Describe the morphology of the red blood cells.
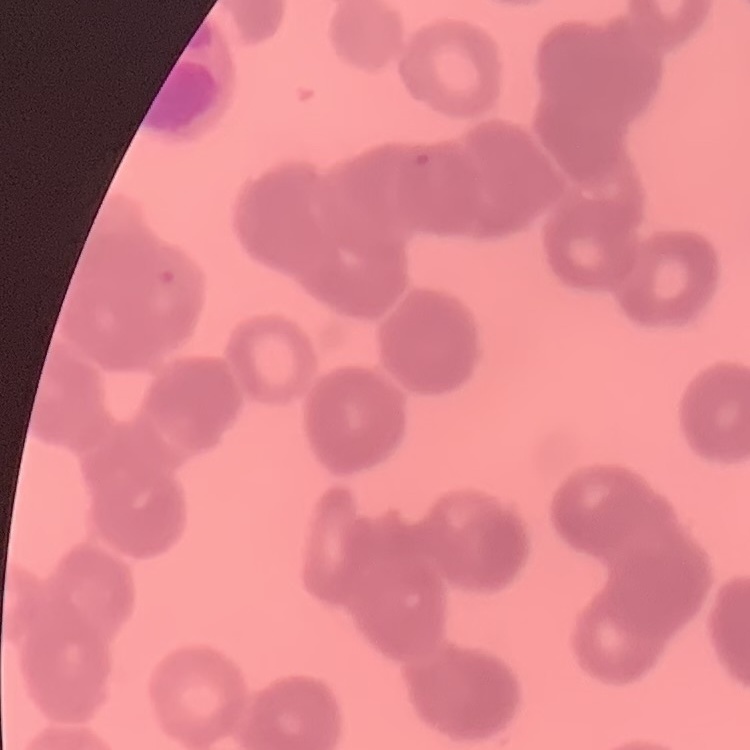

Rouleaux formation.

One tile cut from a larger photomicrograph. Stained with either Field's or Giemsa. Thin peripheral smear.